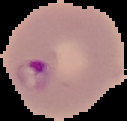

malaria status = parasitized
image size = 127×121 pixels
preparation = thin blood smear
image type = cell region segmented out of the field of view; surrounding area masked to black